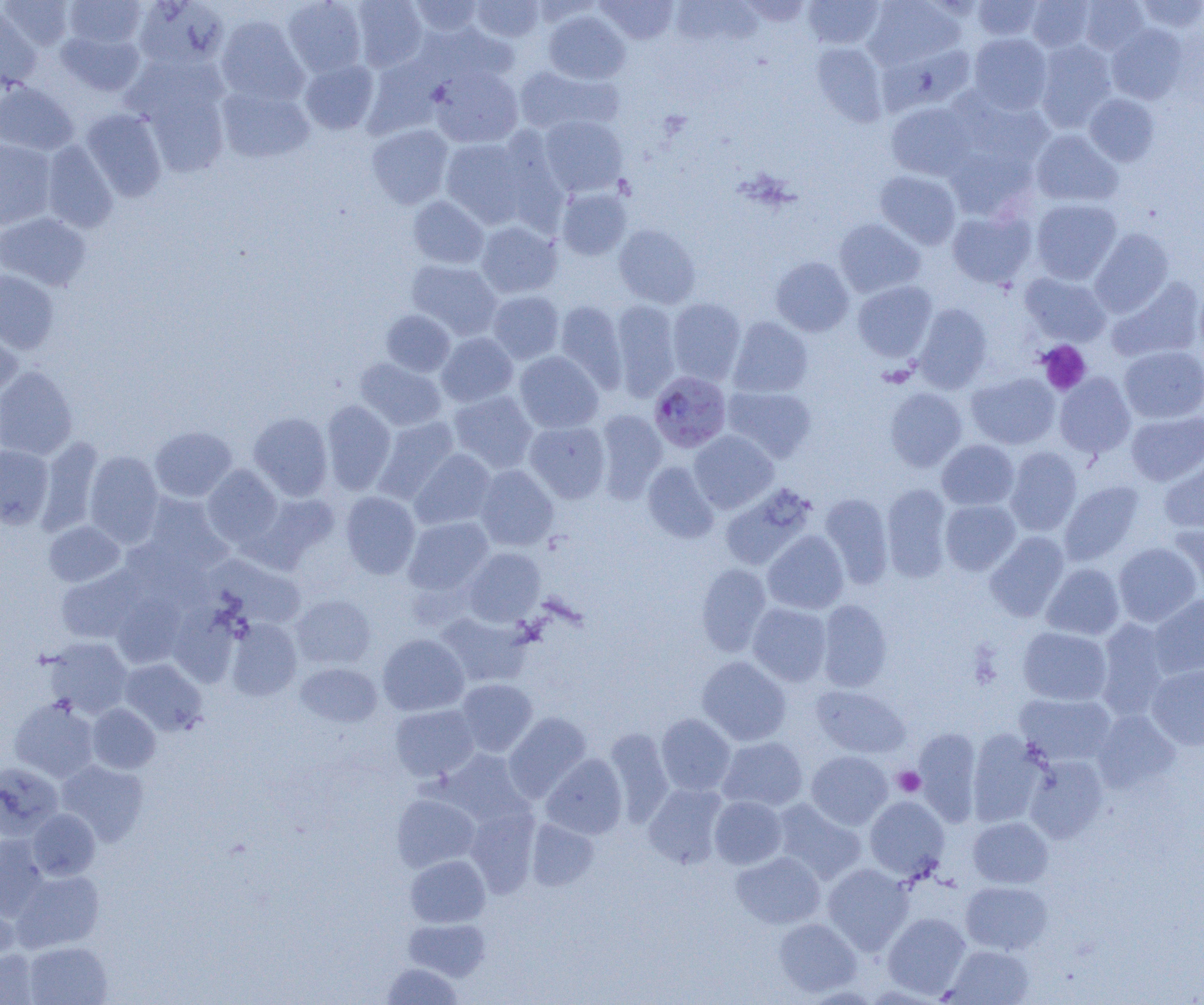
Approximate bounding boxes as (x1, y1, x2, y2) in pixels. Uninfected red blood cell locations: (3, 0, 75, 51), (63, 0, 147, 49), (282, 0, 366, 77), (350, 0, 427, 71), (409, 0, 485, 36), (469, 0, 545, 43), (596, 0, 678, 44), (802, 0, 884, 50), (862, 0, 964, 70), (971, 0, 1045, 41), (1026, 0, 1095, 52), (1078, 0, 1150, 55), (1134, 0, 1204, 33), (133, 1, 230, 70), (671, 1, 759, 48), (0, 7, 42, 90), (543, 11, 630, 84), (216, 15, 309, 105), (419, 22, 515, 87), (1107, 24, 1189, 104), (57, 29, 146, 96), (968, 32, 1053, 115), (1035, 40, 1117, 131), (879, 41, 977, 114), (811, 42, 888, 126), (123, 52, 227, 129), (299, 59, 379, 134), (513, 64, 618, 135), (429, 65, 524, 148), (0, 80, 79, 156), (143, 84, 230, 177), (217, 85, 315, 164), (949, 92, 1053, 171), (1084, 93, 1160, 166), (885, 102, 975, 180), (81, 108, 167, 201), (539, 115, 628, 196), (366, 124, 454, 208), (1031, 129, 1122, 207), (0, 138, 56, 229), (440, 138, 528, 228), (41, 140, 118, 232), (945, 146, 1038, 221), (874, 170, 962, 249), (556, 187, 631, 260), (408, 195, 489, 269), (1031, 199, 1122, 284), (947, 207, 1036, 289), (0, 212, 91, 291), (834, 219, 925, 298), (476, 221, 562, 298), (613, 223, 700, 308), (1090, 228, 1175, 317), (771, 257, 854, 336), (407, 260, 502, 339), (0, 270, 59, 353), (1020, 272, 1111, 346), (1108, 277, 1204, 363), (852, 281, 937, 362), (1194, 282, 1204, 366), (487, 291, 564, 364), (666, 298, 746, 384), (609, 299, 681, 401), (554, 300, 626, 389), (913, 303, 992, 393), (381, 310, 455, 376), (728, 317, 813, 397), (0, 325, 23, 400), (437, 332, 518, 407), (1119, 345, 1204, 423), (514, 350, 603, 433), (355, 357, 446, 431), (0, 365, 78, 460), (967, 372, 1060, 449), (1054, 372, 1136, 459), (722, 386, 817, 462), (885, 388, 967, 472), (448, 390, 537, 473), (321, 400, 396, 495), (593, 409, 667, 502), (1126, 410, 1204, 486), (249, 412, 333, 501), (374, 416, 459, 503), (525, 420, 611, 503), (150, 426, 237, 502), (689, 431, 778, 513), (36, 436, 104, 534), (937, 439, 1019, 510), (0, 445, 53, 528), (1005, 446, 1082, 535), (410, 449, 497, 530), (84, 450, 164, 547), (1159, 454, 1204, 534), (642, 461, 718, 543), (202, 465, 283, 548), (475, 465, 558, 551), (1059, 481, 1143, 565), (881, 483, 953, 582), (720, 484, 816, 570), (340, 491, 420, 578), (253, 492, 340, 567), (139, 493, 232, 574), (820, 494, 893, 587), (940, 500, 1020, 575), (403, 516, 493, 596), (43, 520, 125, 587), (1167, 522, 1204, 600), (762, 530, 849, 614), (985, 532, 1070, 622), (1113, 542, 1201, 627), (463, 547, 545, 626), (205, 553, 306, 629), (696, 563, 772, 656), (1041, 563, 1125, 640), (55, 566, 146, 643), (112, 594, 186, 669), (291, 594, 375, 669), (1148, 594, 1204, 679), (817, 600, 892, 691), (747, 603, 831, 686), (168, 605, 241, 686), (435, 611, 533, 687), (1096, 618, 1172, 718), (226, 619, 302, 700), (1018, 627, 1112, 705), (378, 634, 468, 715), (45, 637, 133, 718), (697, 656, 792, 745), (119, 658, 207, 735), (296, 662, 382, 727), (1147, 663, 1204, 750), (455, 679, 538, 757), (811, 685, 911, 758), (1015, 692, 1116, 765), (10, 697, 100, 782), (87, 703, 160, 773), (390, 704, 480, 782), (1092, 710, 1181, 793), (504, 712, 592, 802), (656, 713, 736, 795), (913, 727, 983, 824), (604, 728, 675, 827), (967, 730, 1048, 826), (717, 736, 808, 811), (437, 748, 530, 826), (806, 750, 893, 830), (542, 753, 627, 839), (1024, 754, 1108, 843), (56, 759, 149, 846), (0, 762, 63, 839), (643, 783, 727, 869), (392, 794, 480, 871), (864, 795, 949, 881), (709, 796, 787, 869), (772, 799, 866, 884), (465, 806, 540, 897), (27, 809, 100, 880), (968, 817, 1053, 888), (527, 819, 598, 891), (0, 834, 50, 921), (731, 852, 826, 929), (405, 855, 490, 927), (822, 863, 914, 955), (11, 870, 105, 953), (961, 881, 1052, 954), (0, 894, 18, 965), (883, 912, 971, 998), (774, 917, 861, 997), (404, 918, 490, 981), (24, 941, 112, 1004), (943, 944, 1034, 1005), (0, 949, 38, 1005), (380, 962, 464, 1004). Plasmodium falciparum-infected red blood cell locations: (649, 371, 731, 452). Platelet locations: (1037, 340, 1091, 395), (893, 766, 925, 797). Slide-level diagnosis: Plasmodium falciparum. Thin blood smear. 1000x magnification. One field of a larger specimen. Image is 1204×1005 pixels. Light microscopy.